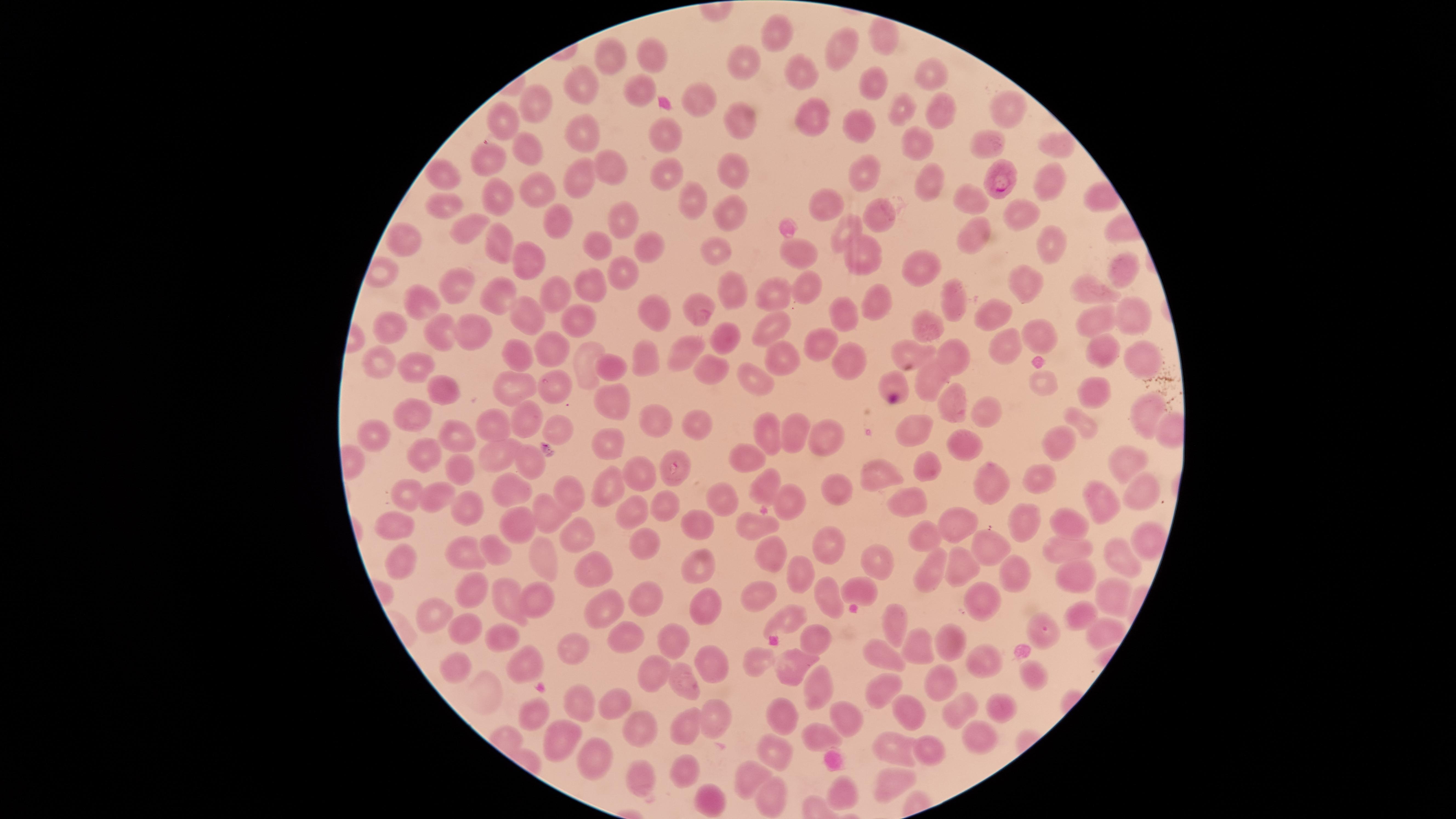

Approximate marker points as (x, y) in pixels. Parasitized RBCs: (1000, 173). Uninfected RBCs: (780, 32), (886, 39), (837, 53), (661, 56), (619, 59), (745, 62), (794, 71), (928, 71), (630, 79), (582, 84), (882, 84), (701, 97), (542, 102), (939, 102), (907, 113), (1010, 115), (504, 116), (812, 120), (863, 123), (742, 126), (593, 133), (666, 134), (918, 140), (1047, 143), (988, 144), (522, 148), (487, 161), (610, 167), (668, 169), (442, 174), (586, 175), (742, 175), (872, 176), (1051, 180), (932, 184), (496, 189), (536, 190), (686, 195), (973, 200), (442, 203), (823, 206), (1019, 213), (737, 216), (877, 216), (557, 217), (626, 217), (461, 220), (844, 229), (971, 238), (599, 242), (503, 244), (1047, 244), (408, 246), (652, 247), (721, 252), (795, 252), (867, 255), (534, 264), (1116, 267), (625, 270), (920, 270), (803, 285), (593, 287), (1016, 287), (462, 289), (1099, 291), (732, 292), (555, 293), (774, 294), (495, 296), (875, 298), (425, 300), (950, 302), (699, 304), (656, 307), (841, 310), (997, 316), (1137, 316), (580, 318), (526, 320), (931, 325), (1095, 326), (396, 327), (771, 327), (445, 335), (473, 335), (722, 336), (1033, 338), (997, 345), (552, 346), (819, 346), (688, 347), (909, 349), (1097, 353), (520, 356), (787, 356), (960, 356), (1137, 357), (854, 360), (383, 362), (590, 362), (652, 362), (612, 365), (716, 369), (422, 370), (934, 375), (758, 377), (1046, 382), (895, 383), (510, 384), (556, 387), (450, 392), (1097, 392), (612, 397), (952, 403), (975, 406), (416, 410), (1147, 411), (525, 413), (651, 418), (1079, 419), (704, 424), (914, 427), (499, 429), (554, 429), (768, 432), (795, 433), (378, 436), (460, 439), (961, 439), (1061, 439), (831, 441), (612, 445), (421, 450), (497, 450), (750, 453), (528, 462), (1120, 462), (925, 469), (877, 470), (676, 472), (458, 475), (643, 477), (1033, 478), (997, 480), (765, 484), (516, 486), (829, 489), (615, 490), (1137, 492), (416, 493), (574, 493), (784, 493), (441, 497), (712, 498), (907, 499), (1099, 503), (470, 508), (547, 508), (633, 508), (665, 512), (1024, 519), (509, 523), (704, 523), (955, 523), (1072, 523), (762, 524), (397, 527), (573, 530), (928, 535), (1148, 537), (645, 543), (830, 546), (1059, 546), (995, 551), (774, 552), (470, 555), (499, 555), (545, 555), (406, 557), (954, 557), (1124, 558), (699, 566), (934, 567), (1016, 567), (882, 568), (588, 574), (807, 576), (1079, 578), (859, 584), (473, 586), (758, 592), (827, 592), (1112, 594), (536, 597), (504, 598), (654, 602), (710, 602), (987, 603), (603, 606), (1079, 612), (440, 617), (786, 617), (904, 620), (1096, 628), (468, 630), (500, 633), (627, 634), (1050, 636), (675, 638), (817, 639), (951, 641), (915, 645), (569, 648), (458, 661), (886, 661), (989, 661), (522, 662), (762, 663), (723, 668), (653, 669), (791, 670), (1031, 676), (684, 681), (886, 684), (947, 686), (817, 687), (996, 700), (577, 703), (617, 705), (959, 708), (534, 714), (909, 714), (712, 715), (840, 716), (791, 718), (684, 725), (827, 731), (640, 732), (554, 736), (977, 737), (929, 751), (896, 752), (775, 754), (596, 760), (685, 769), (747, 775), (892, 778), (648, 781), (842, 791), (775, 798), (710, 800). Single field of view. Thin blood film. Presence: malaria parasites detected. The visible region is circular. Image is 1456×819 pixels. Species: Plasmodium falciparum. Giemsa-stained preparation. Smartphone photograph through the microscope eyepiece.